State which parasite is depicted.
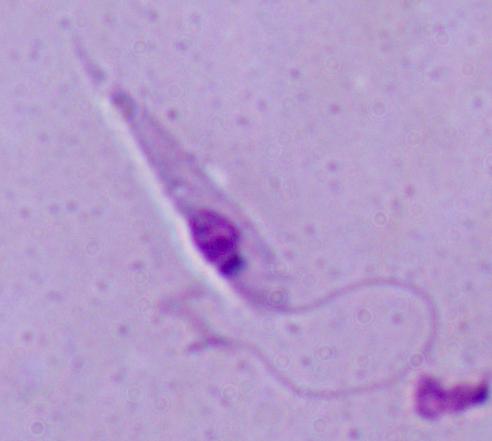

Leishmania.

modality = micrograph
magnification = 1000x